Classify this cell by malaria status.
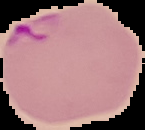

It is parasitized.

Image is 145×130 pixels. From a thin blood film. The area outside the segmented cell region is set to black.